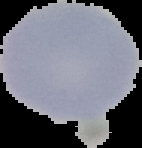

Summary:
  - Preparation: thin blood film
  - Image type: segmented cell region with the area outside set to black
  - Image size: 142×148 pixels
  - Result: negative for Plasmodium parasites